Comment on the morphology of the erythrocytes.
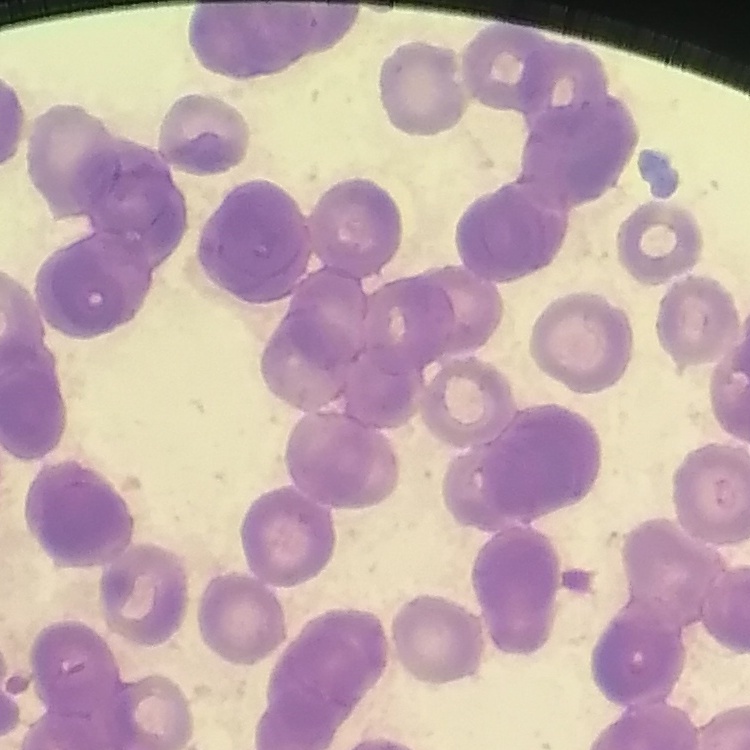
Rouleaux formation.

Summary:
  - Stain: Field's or Giemsa
  - Preparation: thin blood film
  - Image type: one tile cut from a larger photomicrograph